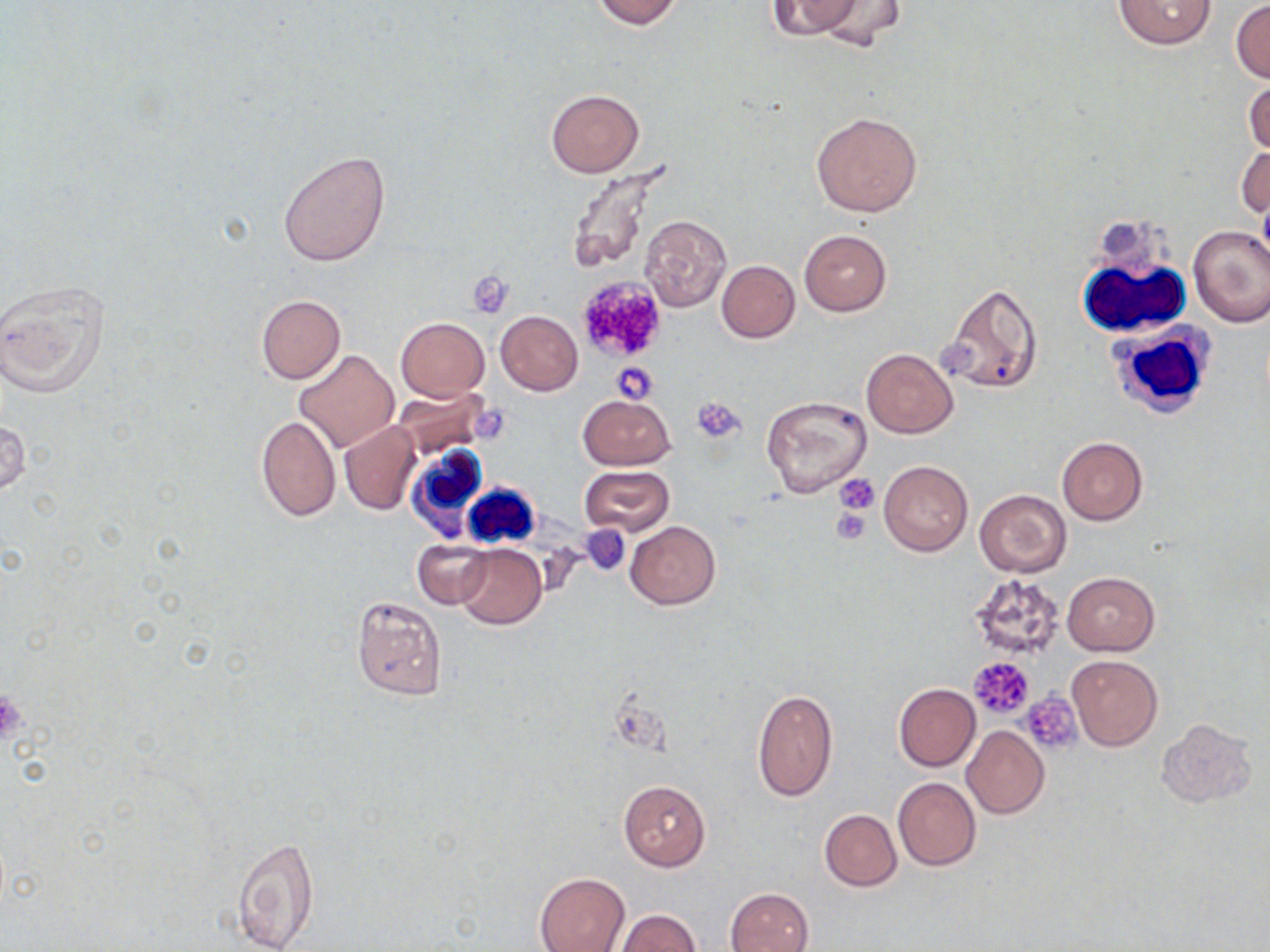
Approximate bounding boxes as [x1, y1, x2, y2] in pixels. Platelet locations: [468, 273, 516, 318], [575, 275, 668, 363], [609, 361, 660, 403], [692, 396, 746, 443], [835, 474, 879, 514], [830, 507, 872, 544], [581, 526, 632, 575], [968, 656, 1034, 718], [0, 687, 28, 747], [1019, 692, 1083, 754]. White blood cell locations: [1075, 219, 1191, 338], [1108, 321, 1214, 420], [407, 443, 491, 533], [462, 482, 540, 551]. Uninfected red blood cell locations: [591, 0, 685, 30], [766, 0, 866, 39], [805, 0, 909, 49], [1112, 0, 1217, 50], [1231, 0, 1270, 83], [1244, 75, 1270, 158], [546, 88, 645, 178], [811, 110, 923, 217], [1237, 143, 1269, 221], [278, 150, 391, 266], [566, 162, 675, 276], [639, 215, 732, 314], [1187, 225, 1270, 327], [799, 230, 891, 317], [717, 260, 799, 342], [0, 276, 110, 401], [941, 283, 1044, 395], [255, 295, 346, 384], [495, 310, 583, 395], [395, 317, 489, 402], [862, 349, 957, 437], [293, 350, 398, 453], [392, 386, 494, 462], [579, 394, 676, 469], [761, 396, 872, 499], [255, 414, 340, 522], [0, 416, 29, 501], [339, 420, 422, 515], [1057, 436, 1147, 526], [879, 461, 972, 556], [581, 465, 675, 537], [975, 489, 1071, 577], [625, 521, 719, 609], [412, 539, 490, 608], [454, 543, 545, 629], [1062, 572, 1159, 655], [969, 573, 1069, 661], [351, 595, 447, 700], [1067, 654, 1163, 751], [893, 683, 981, 772], [752, 688, 839, 803], [1156, 718, 1258, 807], [962, 726, 1049, 818], [892, 778, 981, 870], [620, 781, 710, 871], [819, 809, 902, 891], [231, 837, 320, 950], [535, 872, 630, 952], [725, 888, 813, 952], [614, 910, 702, 952]. Slide-level diagnosis: no evidence of blood parasites. Thin blood film. Image is 1270×952 pixels. Optical microscopy. Captured at 1000x magnification. May-Grünwald-Giemsa-stained preparation. One field of a larger specimen.